Identify the blood parasite species.
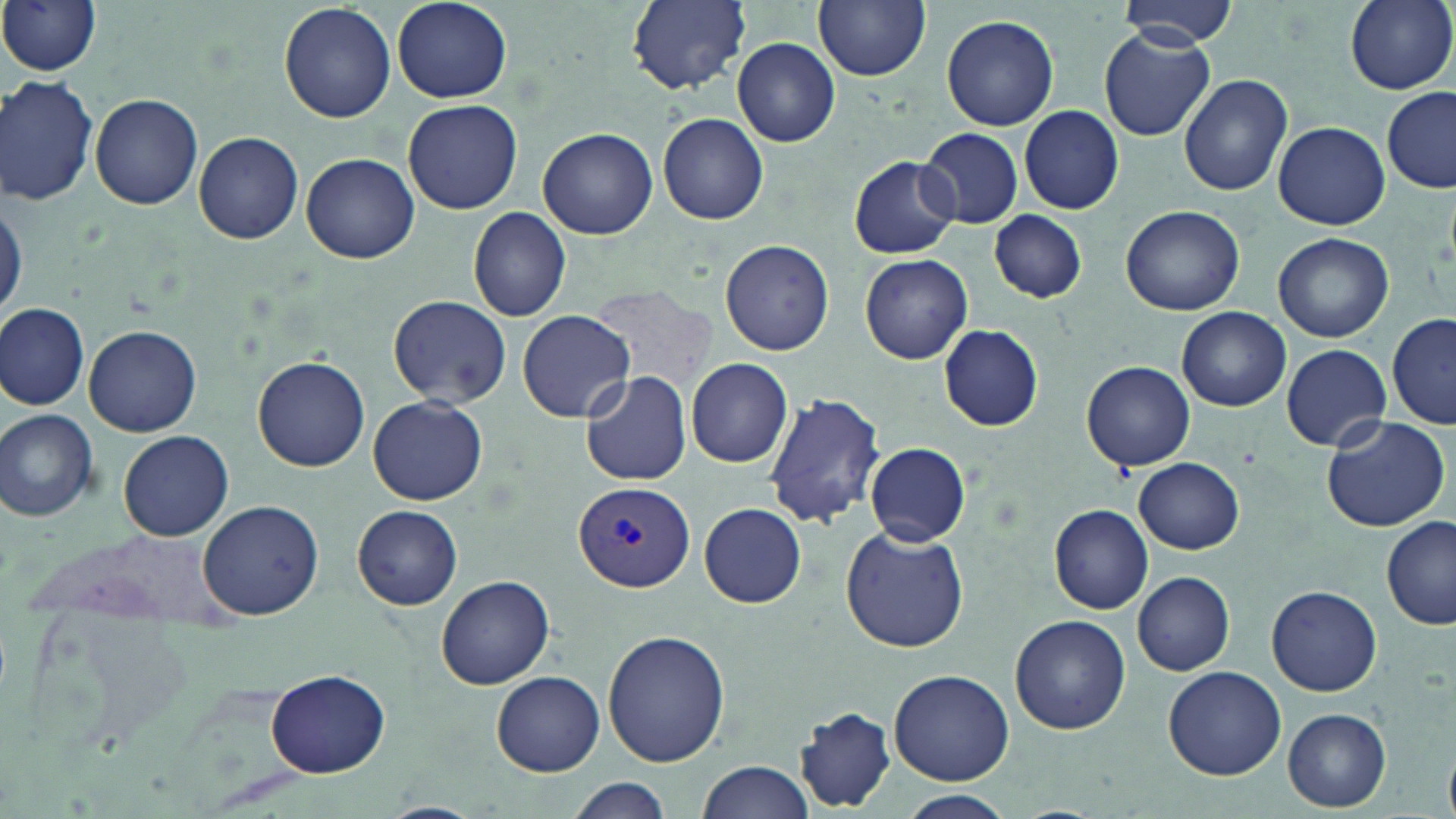

Plasmodium vivax.

Summary:
  - Coordinate format: approximate bounding boxes as (x1,y1)-(x2,y2) corner pairs in pixels
  - Plasmodium vivax-infected red blood cell locations: (575,480)-(695,593)
  - Uninfected red blood cell locations: (0,0)-(103,76), (625,0)-(752,94), (813,0)-(930,80), (1114,0)-(1237,47), (1345,0)-(1455,93), (390,1)-(512,103), (279,2)-(395,124), (942,13)-(1060,131), (1099,29)-(1214,142), (733,38)-(840,147), (1179,72)-(1295,196), (1,73)-(99,208), (1380,88)-(1456,193), (89,94)-(203,209), (402,99)-(523,215), (1019,105)-(1124,215), (659,111)-(769,225), (1274,121)-(1390,230), (537,127)-(657,240), (918,127)-(1024,228), (193,132)-(304,244), (301,152)-(420,264), (848,154)-(961,259), (1,195)-(25,322), (1121,205)-(1245,315), (468,206)-(572,323), (989,210)-(1087,303), (1273,232)-(1394,343), (719,240)-(834,355), (859,254)-(973,365), (386,294)-(511,406), (0,302)-(89,411), (1177,307)-(1289,412), (517,310)-(634,422), (1388,314)-(1455,429), (82,323)-(202,436), (938,324)-(1044,432), (1280,343)-(1392,452), (253,355)-(370,471), (685,358)-(793,468), (1081,361)-(1195,473), (580,371)-(692,486), (763,391)-(886,529), (369,395)-(488,505), (0,409)-(101,522), (1319,416)-(1451,533), (118,430)-(234,540), (864,441)-(970,546), (1134,457)-(1244,554), (197,499)-(324,619), (699,503)-(807,607), (1048,503)-(1155,615), (351,504)-(463,610), (1382,516)-(1456,629), (839,526)-(969,653), (1133,572)-(1235,675), (436,574)-(555,689), (1266,584)-(1382,696), (1010,614)-(1129,735), (601,629)-(731,767), (1162,667)-(1287,780), (266,669)-(389,778), (889,669)-(1014,785), (493,671)-(604,776), (791,705)-(899,812), (1282,708)-(1390,812), (698,760)-(814,817), (567,778)-(675,818), (902,790)-(1014,817), (376,802)-(485,819)
  - Magnification: 1000x
  - Field of view: one of a larger specimen
  - Image size: 1456×819 pixels
  - Modality: optical microscopy
  - Stain: May-Grünwald-Giemsa
  - Preparation: thin blood film